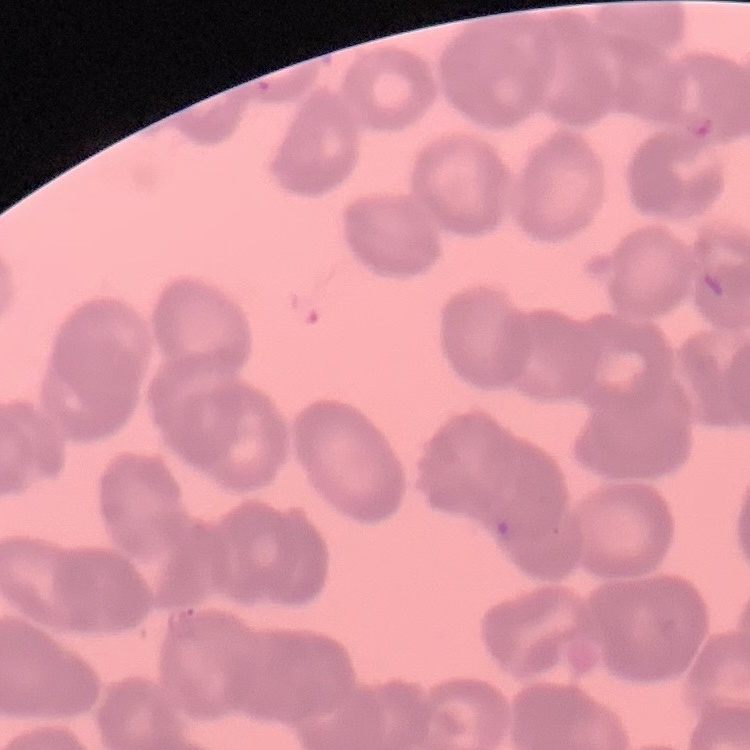
erythrocyte_morphology: rouleaux formation
stain: Field's or Giemsa
image_type: square crop of a larger photomicrograph
preparation: thin blood film